Assess the morphology of the erythrocytes.
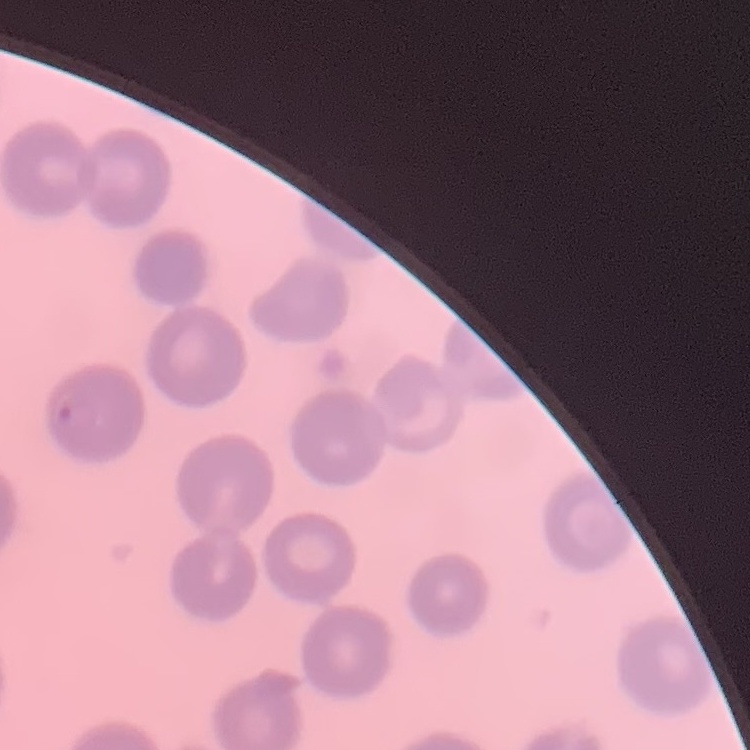

No rouleaux formation.

preparation = thin blood smear
stain = Field's or Giemsa
image type = square crop of a larger photomicrograph